Locate every Plasmodium parasite.
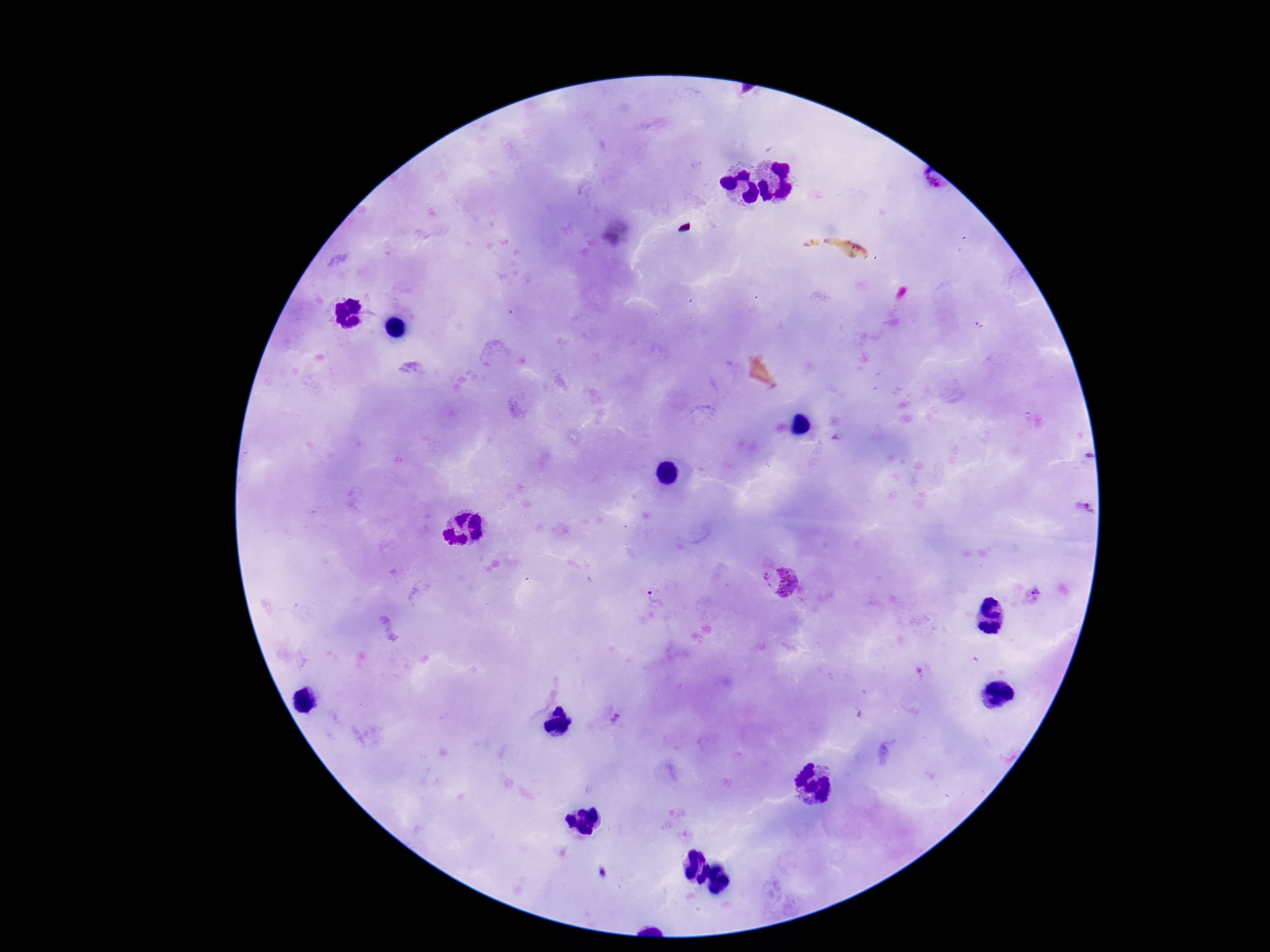
Approximate centers as (x, y) in pixels.
Plasmodium parasites: (932, 183), (1087, 507), (777, 582), (1033, 595), (653, 596), (616, 719).

Summary:
  - Patient malaria status: positive
  - Stain: Giemsa
  - Magnification: 100x
  - Image size: 1270×952 pixels
  - Preparation: thick blood film
  - Capture: smartphone camera through the microscope eyepiece
  - Field of view: single